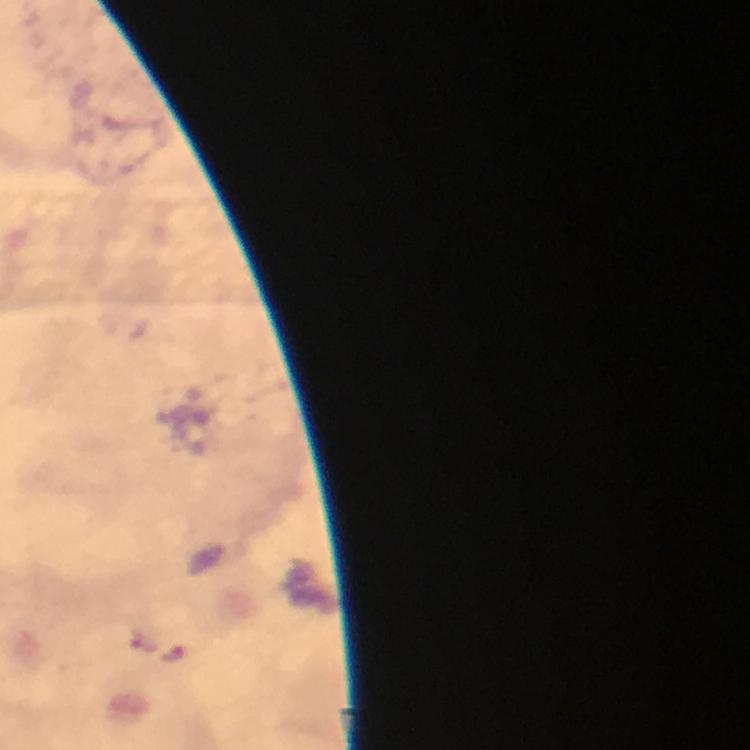

Approximate centers as (x, y) in pixels. Malaria parasite locations: (172, 654). Thick smear. 100x magnification. Image is 750×750 pixels. Giemsa stain. A crop from one field of view. Smartphone photograph taken through a microscope. Immersion oil applied. From a diagnostic examination for malaria.